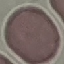
Malaria status: uninfected. Acquired by smartphone through the microscope eyepiece. Giemsa-stained preparation. Automatically extracted cell patch, resized to 64 × 64 pixels. Thin blood smear.